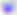

Summary:
  - Identification: Toxoplasma gondii
  - Modality: photomicrograph
  - Magnification: 400x